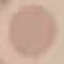

Malaria status: uninfected. Photographed with a smartphone camera at the microscope eyepiece. Thin blood smear. Cell patch, automatically extracted from a larger field of view and resized to 64 × 64 pixels. Giemsa-stained preparation.